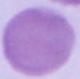 A red blood cell is seen. 1000x magnification. Micrograph.